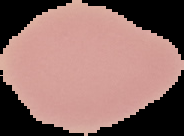

image_type: cell region segmented out of the field of view; surrounding area masked to black
malaria_status: uninfected
image_size: 184×136 pixels
preparation: thin blood film